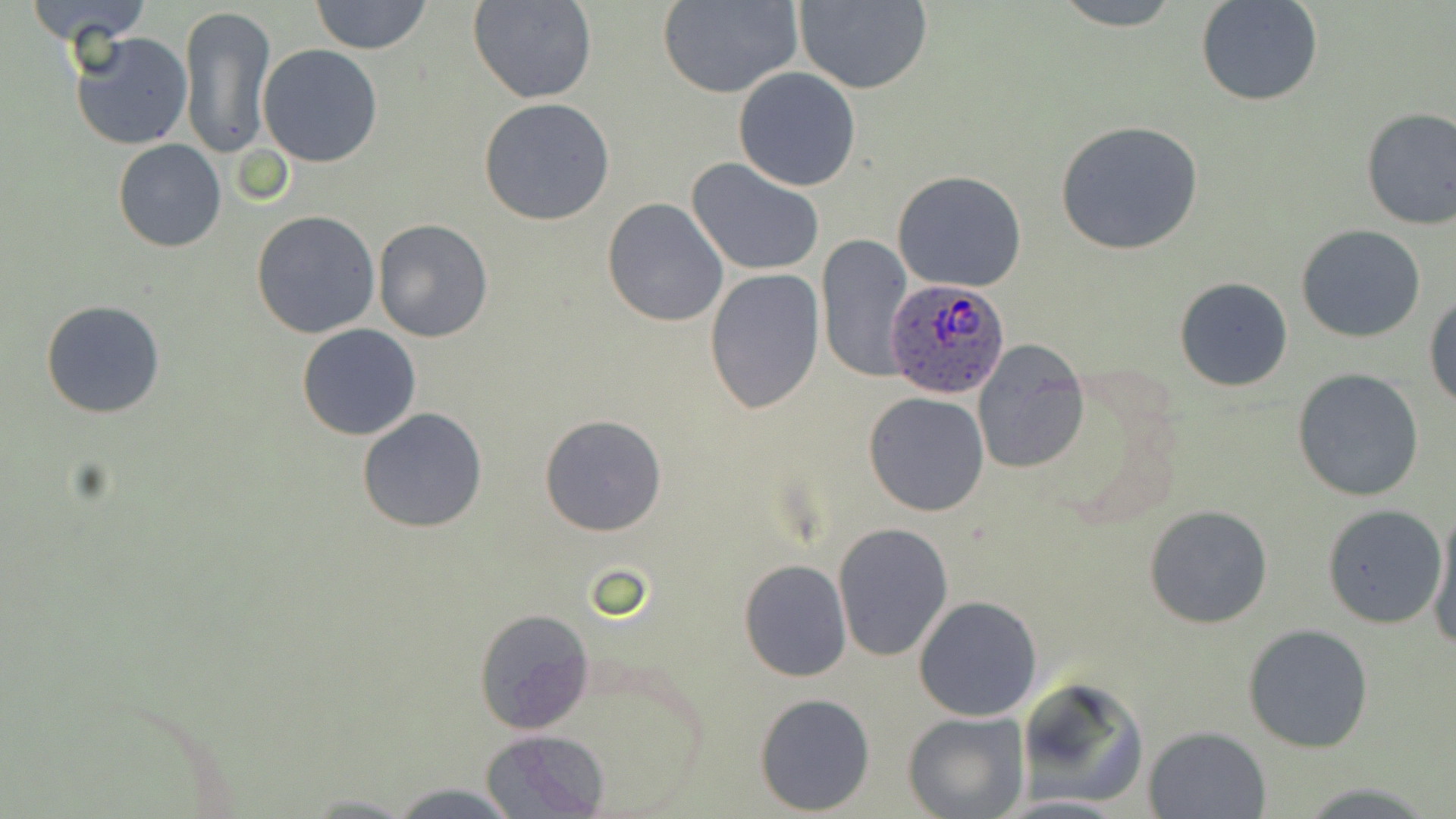 Approximate bounding boxes as (x1, y1, x2, y2) in pixels. Uninfected red blood cell locations: (18, 0, 155, 48), (311, 0, 432, 55), (469, 0, 598, 104), (658, 0, 803, 99), (793, 0, 933, 94), (1051, 0, 1186, 30), (1197, 0, 1324, 107), (177, 4, 276, 161), (69, 31, 193, 151), (258, 45, 384, 166), (732, 67, 861, 192), (478, 97, 618, 226), (1359, 107, 1455, 230), (1054, 120, 1205, 255), (113, 139, 226, 252), (686, 159, 825, 275), (893, 170, 1027, 293), (602, 197, 730, 326), (251, 211, 380, 339), (373, 219, 493, 342), (1297, 224, 1426, 343), (816, 235, 914, 381), (704, 268, 824, 416), (1174, 276, 1293, 391), (1425, 292, 1456, 409), (41, 300, 167, 419), (296, 324, 422, 441), (972, 340, 1090, 475), (1293, 368, 1425, 501), (863, 391, 991, 516), (358, 407, 488, 533), (539, 415, 667, 537), (1321, 503, 1447, 629), (1144, 504, 1271, 630), (1428, 510, 1456, 651), (832, 521, 953, 663), (739, 559, 851, 682), (913, 596, 1042, 723), (473, 608, 595, 734), (1243, 623, 1374, 752), (1013, 679, 1149, 809), (753, 692, 875, 814), (904, 711, 1028, 819), (1144, 725, 1272, 818), (481, 731, 611, 817), (382, 780, 526, 818). Plasmodium ovale-infected red blood cell locations: (886, 279, 1009, 398). Slide-level diagnosis: Plasmodium ovale. May-Grünwald-Giemsa stain. Single field of view. Thin blood film. Image is 1456×819 pixels. Light microscopy. Captured at 1000x magnification.